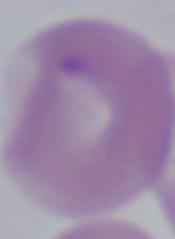
Summary:
  - Identification: Babesia
  - Magnification: 1000x
  - Modality: photomicrograph